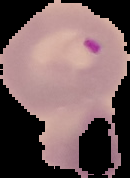

malaria status = parasitized
image size = 130×178 pixels
preparation = thin blood film
image type = segmented cell region with the area outside set to black